Locate every Plasmodium ovale-infected red blood cell.
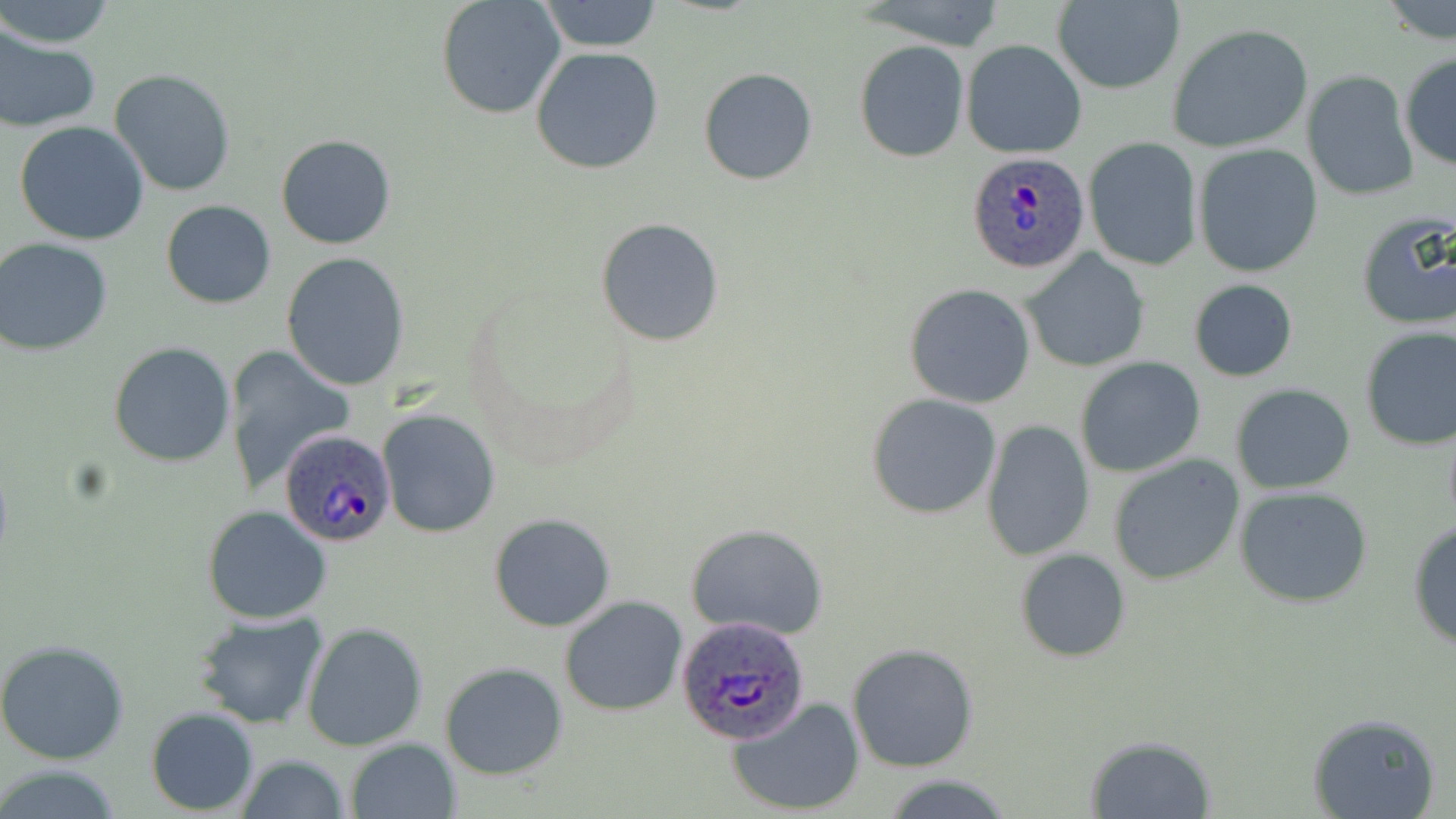

Approximate bounding boxes as named x1/y1/x2/y2 corners in pixels.
Plasmodium ovale-infected red blood cells: (x1=967, y1=152, x2=1092, y2=275), (x1=280, y1=428, x2=396, y2=547), (x1=678, y1=616, x2=812, y2=746).

slide-level diagnosis = Plasmodium ovale
field of view = one of a larger specimen
preparation = thin blood film
modality = optical microscopy
stain = May-Grünwald-Giemsa
uninfected red blood cell locations = approximate bounding boxes as named x1/y1/x2/y2 corners in pixels: (x1=434, y1=0, x2=566, y2=119), (x1=537, y1=0, x2=662, y2=53), (x1=2, y1=1, x2=116, y2=48), (x1=1049, y1=1, x2=1184, y2=95), (x1=1379, y1=1, x2=1456, y2=46), (x1=1166, y1=22, x2=1315, y2=154), (x1=0, y1=29, x2=100, y2=132), (x1=962, y1=39, x2=1086, y2=159), (x1=854, y1=40, x2=969, y2=163), (x1=531, y1=46, x2=663, y2=175), (x1=1399, y1=51, x2=1456, y2=171), (x1=698, y1=67, x2=817, y2=185), (x1=109, y1=70, x2=236, y2=196), (x1=1302, y1=71, x2=1419, y2=201), (x1=13, y1=120, x2=151, y2=245), (x1=276, y1=134, x2=398, y2=250), (x1=1083, y1=135, x2=1201, y2=271), (x1=1193, y1=144, x2=1322, y2=278), (x1=161, y1=201, x2=275, y2=308), (x1=1353, y1=209, x2=1456, y2=333), (x1=595, y1=216, x2=725, y2=348), (x1=0, y1=238, x2=113, y2=355), (x1=1021, y1=250, x2=1151, y2=372), (x1=281, y1=252, x2=411, y2=391), (x1=1189, y1=280, x2=1297, y2=382), (x1=905, y1=283, x2=1035, y2=408), (x1=1359, y1=325, x2=1456, y2=450), (x1=107, y1=343, x2=236, y2=466), (x1=222, y1=346, x2=356, y2=491), (x1=1075, y1=357, x2=1206, y2=478), (x1=1231, y1=383, x2=1357, y2=495), (x1=866, y1=393, x2=1002, y2=520), (x1=378, y1=409, x2=501, y2=538), (x1=981, y1=420, x2=1095, y2=562), (x1=1106, y1=453, x2=1246, y2=586), (x1=1235, y1=488, x2=1374, y2=608), (x1=202, y1=506, x2=333, y2=624), (x1=488, y1=514, x2=617, y2=631), (x1=1406, y1=514, x2=1456, y2=652), (x1=684, y1=522, x2=828, y2=641), (x1=1015, y1=548, x2=1131, y2=663), (x1=559, y1=595, x2=688, y2=717), (x1=193, y1=610, x2=332, y2=731), (x1=302, y1=621, x2=428, y2=753), (x1=0, y1=639, x2=130, y2=764), (x1=847, y1=642, x2=979, y2=772), (x1=439, y1=662, x2=568, y2=780), (x1=728, y1=696, x2=866, y2=817), (x1=145, y1=707, x2=260, y2=815), (x1=1306, y1=710, x2=1441, y2=819), (x1=1084, y1=735, x2=1215, y2=817), (x1=344, y1=737, x2=460, y2=819), (x1=235, y1=754, x2=350, y2=819), (x1=0, y1=762, x2=127, y2=819)
magnification = 1000x
image size = 1456×819 pixels